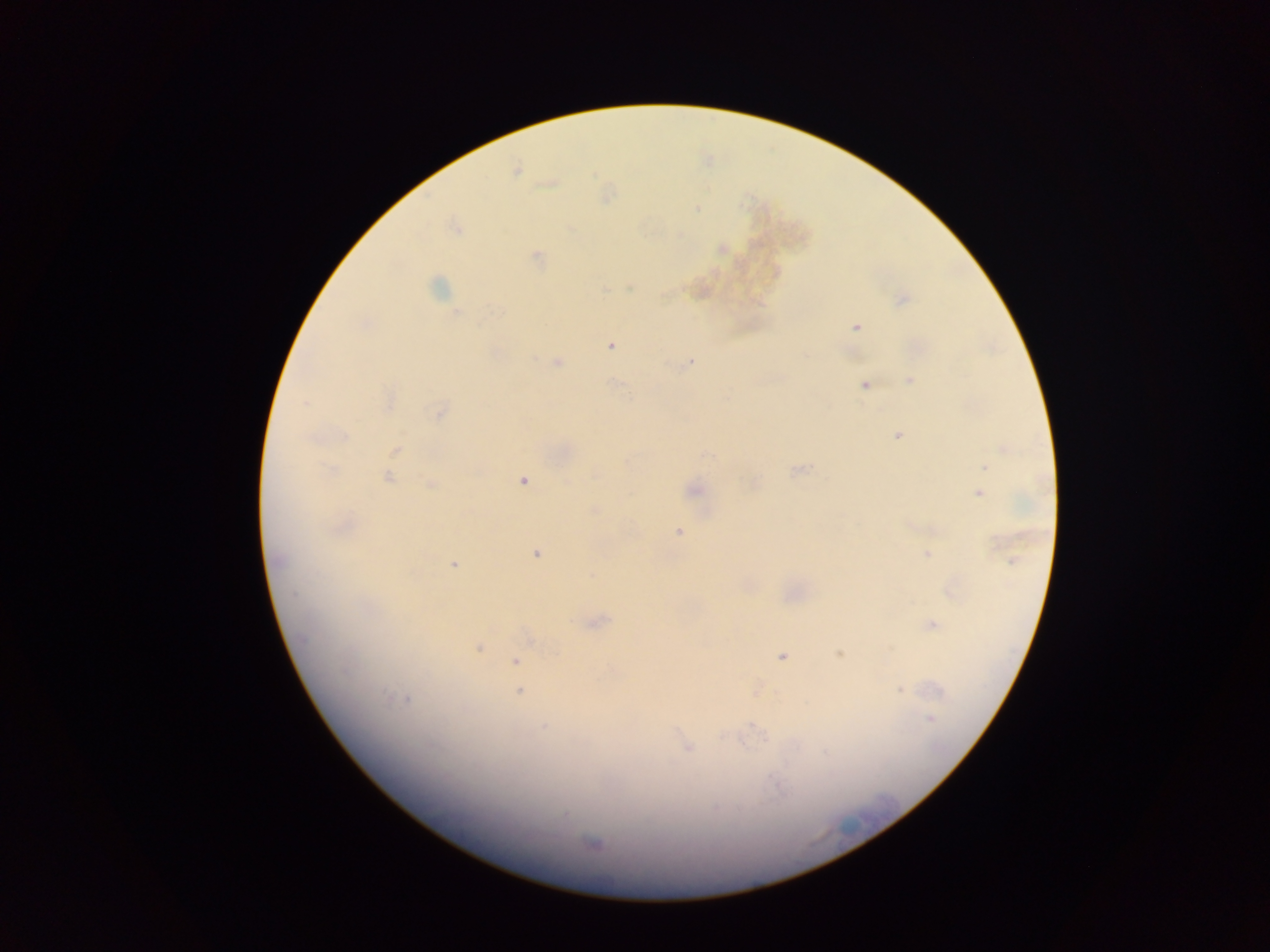
Approximate centers as {x, y} in pixels. Plasmodium parasite locations: {516, 171}, {695, 210}, {572, 229}, {681, 233}, {537, 257}, {438, 286}, {631, 286}, {605, 290}, {665, 296}, {902, 298}, {854, 327}, {610, 344}, {534, 358}, {559, 360}, {690, 360}, {909, 378}, {612, 382}, {864, 386}, {306, 402}, {438, 410}, {897, 435}, {394, 449}, {985, 466}, {794, 470}, {593, 473}, {388, 477}, {523, 482}, {694, 488}, {979, 495}, {677, 532}, {926, 553}, {535, 554}, {274, 560}, {453, 564}, {590, 575}, {596, 620}, {932, 624}, {479, 647}, {890, 650}, {837, 654}, {782, 656}, {516, 660}, {519, 690}, {900, 690}, {389, 696}, {408, 700}, {930, 717}, {751, 724}, {545, 726}, {724, 738}, {765, 741}, {741, 742}, {687, 748}, {824, 755}, {594, 844}. Thick blood film. Image is 1270×952 pixels. Mobile-phone photograph taken through the microscope. Sample from Ghana. One field of view.